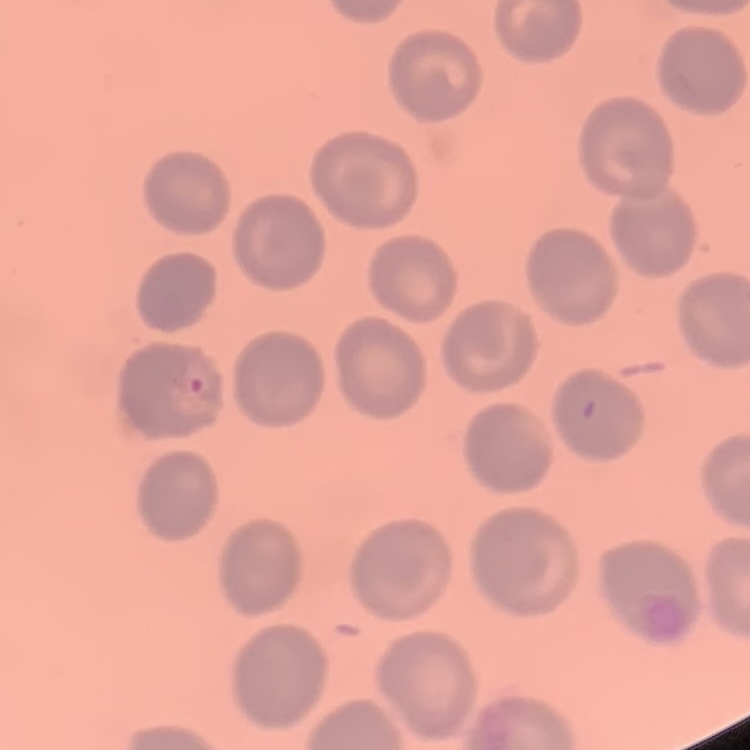
red blood cell morphology = no rouleaux formation
preparation = thin blood film
stain = Field's or Giemsa
image type = square crop of a larger photomicrograph